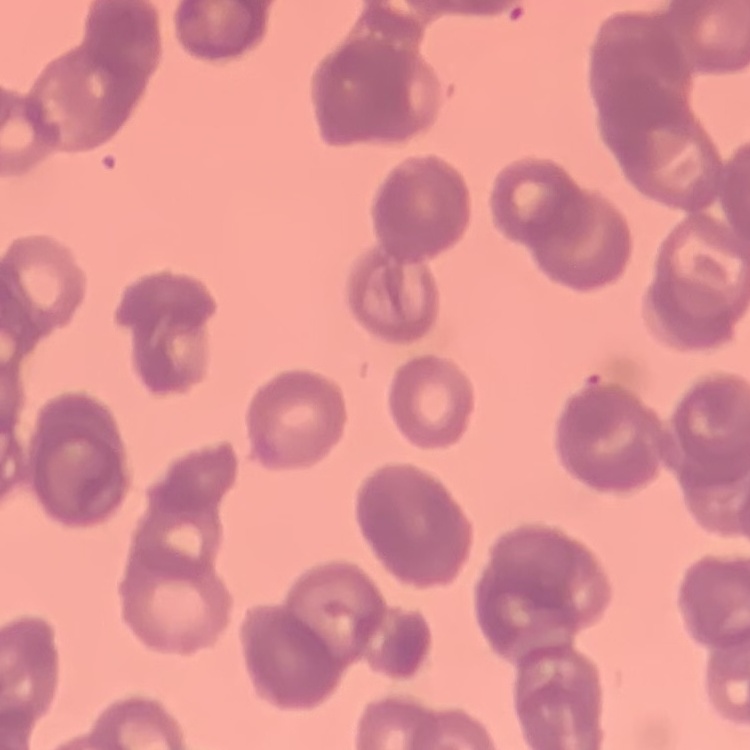
Summary:
  - Red blood cell morphology: rouleaux formation
  - Image type: square crop of a larger photomicrograph
  - Preparation: thin peripheral smear
  - Stain: Field's or Giemsa